Assess this cell for malaria.
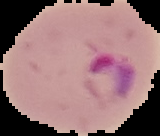
Parasitized.

Segmented cell region on a black background. Image is 160×136 pixels. From a thin blood film.